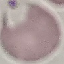
{
  "result": "no malaria parasites detected",
  "preparation": "thin blood film",
  "image_type": "cell patch, automatically extracted from a larger field of view and resized to 64 × 64 pixels",
  "stain": "Giemsa",
  "capture": "smartphone through the microscope eyepiece"
}